Identify the blood parasite species.
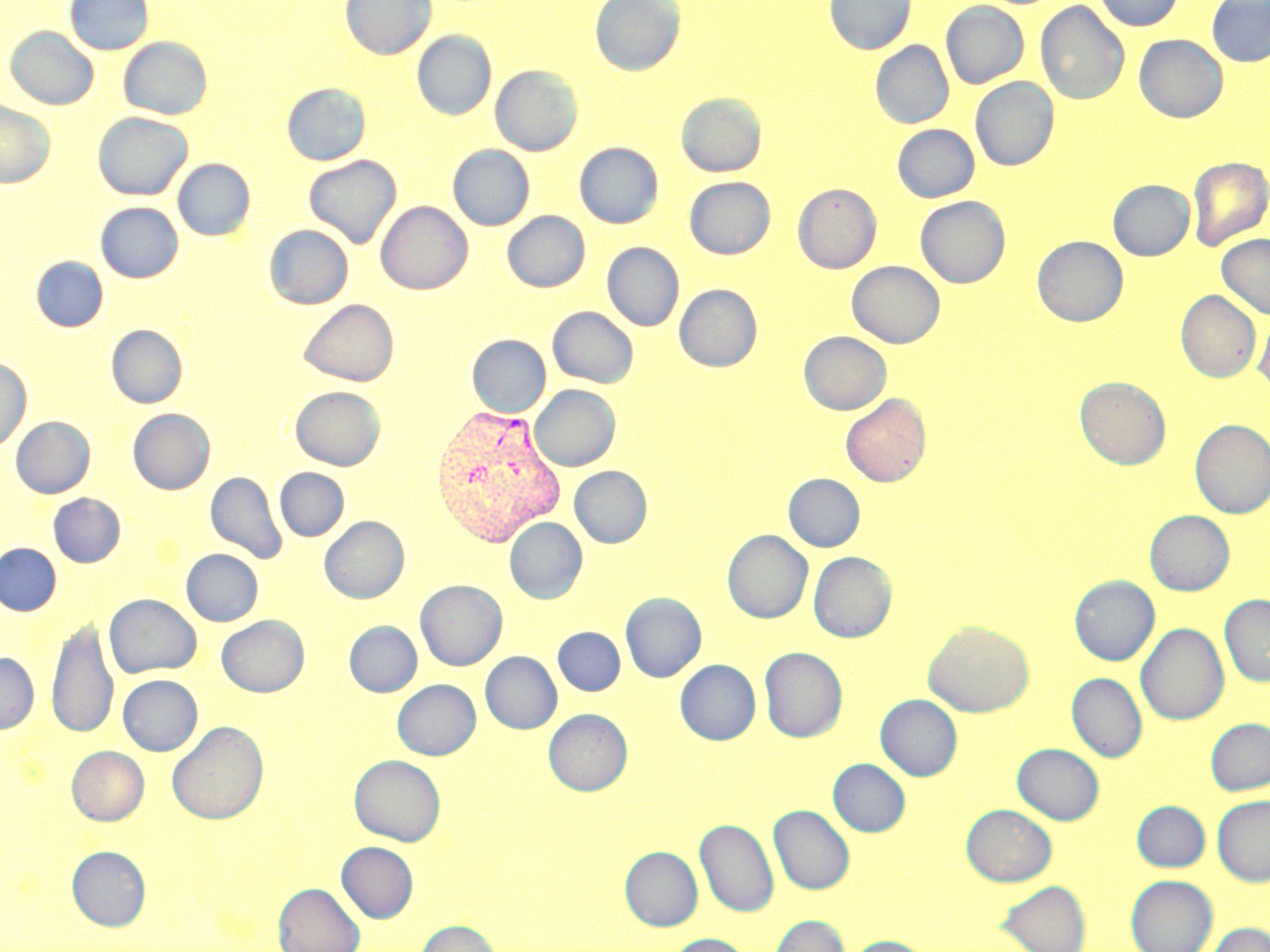
Plasmodium vivax.

image_size: 1270×952 pixels
plasmodium_vivax_infected_red_blood_cell_locations: 'approximate bounding boxes as named x1/y1/x2/y2 corners in pixels: (x1=430, y1=403, x2=565, y2=548)'
magnification: 1000x
preparation: thin blood film
modality: optical microscopy
field_of_view: one of a larger specimen
stain: May-Grünwald-Giemsa
uninfected_red_blood_cell_locations: 'approximate bounding boxes as named x1/y1/x2/y2 corners in pixels: (x1=65, y1=0, x2=153, y2=55), (x1=341, y1=0, x2=436, y2=59), (x1=590, y1=0, x2=685, y2=76), (x1=825, y1=0, x2=915, y2=55), (x1=1094, y1=0, x2=1182, y2=31), (x1=941, y1=1, x2=1029, y2=88), (x1=1035, y1=1, x2=1130, y2=105), (x1=1207, y1=1, x2=1270, y2=66), (x1=5, y1=27, x2=98, y2=109), (x1=412, y1=31, x2=496, y2=120), (x1=1134, y1=35, x2=1228, y2=122), (x1=119, y1=37, x2=212, y2=120), (x1=871, y1=41, x2=954, y2=128), (x1=490, y1=65, x2=582, y2=156), (x1=971, y1=78, x2=1058, y2=171), (x1=281, y1=83, x2=371, y2=166), (x1=676, y1=93, x2=766, y2=177), (x1=0, y1=100, x2=55, y2=187), (x1=92, y1=112, x2=193, y2=200), (x1=892, y1=124, x2=979, y2=202), (x1=575, y1=143, x2=663, y2=228), (x1=448, y1=145, x2=534, y2=230), (x1=304, y1=154, x2=401, y2=248), (x1=1187, y1=156, x2=1270, y2=250), (x1=173, y1=158, x2=255, y2=240), (x1=684, y1=177, x2=775, y2=259), (x1=1108, y1=180, x2=1194, y2=260), (x1=793, y1=184, x2=881, y2=273), (x1=915, y1=196, x2=1010, y2=288), (x1=376, y1=201, x2=472, y2=294), (x1=96, y1=202, x2=183, y2=282), (x1=503, y1=211, x2=589, y2=292), (x1=265, y1=225, x2=353, y2=309), (x1=1217, y1=233, x2=1270, y2=320), (x1=1032, y1=236, x2=1128, y2=326), (x1=602, y1=243, x2=684, y2=331), (x1=31, y1=257, x2=108, y2=332), (x1=847, y1=261, x2=945, y2=348), (x1=675, y1=284, x2=762, y2=371), (x1=1176, y1=290, x2=1261, y2=383), (x1=298, y1=299, x2=399, y2=387), (x1=548, y1=307, x2=638, y2=388), (x1=1253, y1=312, x2=1270, y2=395), (x1=107, y1=325, x2=187, y2=408), (x1=799, y1=331, x2=890, y2=414), (x1=468, y1=335, x2=550, y2=417), (x1=0, y1=357, x2=31, y2=453), (x1=1074, y1=377, x2=1170, y2=469), (x1=530, y1=385, x2=620, y2=471), (x1=290, y1=386, x2=385, y2=470), (x1=840, y1=393, x2=931, y2=487), (x1=128, y1=409, x2=215, y2=494), (x1=10, y1=416, x2=95, y2=498), (x1=1190, y1=420, x2=1270, y2=518), (x1=569, y1=466, x2=652, y2=547), (x1=275, y1=468, x2=349, y2=541), (x1=205, y1=471, x2=287, y2=564), (x1=784, y1=474, x2=865, y2=551), (x1=49, y1=493, x2=125, y2=567), (x1=1145, y1=510, x2=1234, y2=595), (x1=319, y1=516, x2=408, y2=603), (x1=504, y1=517, x2=587, y2=603), (x1=722, y1=530, x2=812, y2=623), (x1=0, y1=543, x2=61, y2=615), (x1=181, y1=549, x2=263, y2=625), (x1=808, y1=551, x2=896, y2=642), (x1=1070, y1=575, x2=1159, y2=665), (x1=416, y1=580, x2=506, y2=670), (x1=621, y1=592, x2=706, y2=682), (x1=105, y1=594, x2=201, y2=678), (x1=1219, y1=594, x2=1270, y2=687), (x1=217, y1=615, x2=309, y2=697), (x1=47, y1=618, x2=118, y2=741), (x1=345, y1=621, x2=422, y2=696), (x1=923, y1=621, x2=1034, y2=717), (x1=1136, y1=623, x2=1229, y2=725), (x1=554, y1=627, x2=625, y2=695), (x1=759, y1=647, x2=847, y2=742), (x1=480, y1=652, x2=562, y2=733), (x1=0, y1=653, x2=38, y2=734), (x1=675, y1=659, x2=760, y2=745), (x1=1067, y1=673, x2=1147, y2=762), (x1=117, y1=675, x2=202, y2=755), (x1=393, y1=679, x2=480, y2=759), (x1=876, y1=695, x2=962, y2=781), (x1=544, y1=709, x2=632, y2=795), (x1=1205, y1=719, x2=1270, y2=795), (x1=167, y1=721, x2=268, y2=825), (x1=1013, y1=743, x2=1104, y2=824), (x1=67, y1=745, x2=149, y2=825), (x1=349, y1=755, x2=445, y2=846), (x1=828, y1=759, x2=910, y2=836), (x1=1212, y1=795, x2=1270, y2=886), (x1=1132, y1=801, x2=1209, y2=871), (x1=962, y1=804, x2=1057, y2=886), (x1=769, y1=805, x2=854, y2=895), (x1=695, y1=819, x2=778, y2=917), (x1=337, y1=842, x2=417, y2=922), (x1=66, y1=846, x2=150, y2=931), (x1=620, y1=846, x2=703, y2=930), (x1=1126, y1=875, x2=1218, y2=952), (x1=997, y1=880, x2=1091, y2=952), (x1=273, y1=883, x2=364, y2=952), (x1=769, y1=915, x2=850, y2=952), (x1=415, y1=919, x2=501, y2=952), (x1=1205, y1=923, x2=1270, y2=952), (x1=665, y1=934, x2=753, y2=952), (x1=841, y1=936, x2=935, y2=952)'